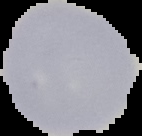
The area outside the segmented cell region is set to black. Image is 142×136 pixels. Malaria status: uninfected. From a thin blood film.